Identify the parasite.
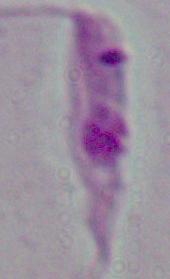
This is Leishmania.

Summary:
  - Modality: photomicrograph
  - Magnification: 1000x